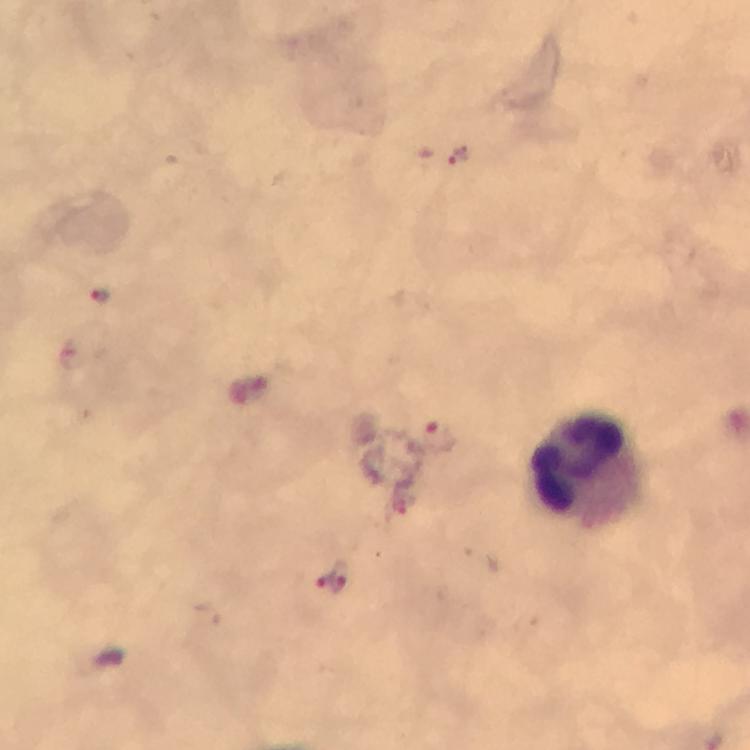
Approximate object centers, in pixels from the top-left corner.
Summary:
  - Leukocyte locations: (x=589, y=470)
  - Plasmodium parasite locations: (x=463, y=159), (x=101, y=295), (x=248, y=391), (x=429, y=439), (x=333, y=575)
  - Capture: smartphone mounted on the microscope
  - Preparation: thick blood film
  - Stain: Giemsa
  - Magnification: 100x
  - Context: from a malaria diagnostic workup
  - Image size: 750×750 pixels
  - Cropped from: a single field of view
  - Immersion oil: used